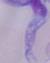
Summary:
  - Modality: photomicrograph
  - Identification: trypanosome
  - Magnification: 1000x